Describe the morphology of the erythrocytes.
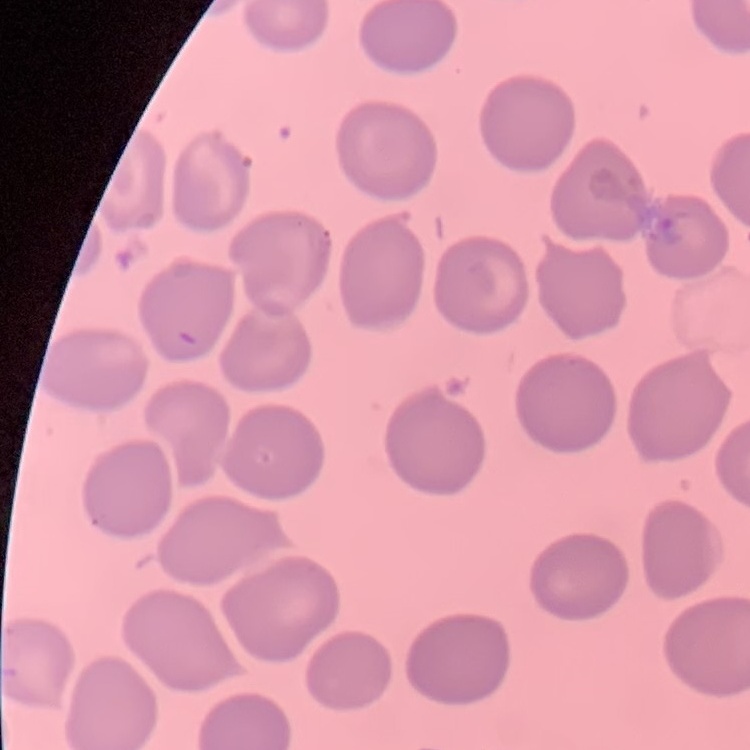
They show no rouleaux formation.

Stained with either Field's or Giemsa. Square crop of a larger photomicrograph. Thin blood smear.